Look for Plasmodium parasites.
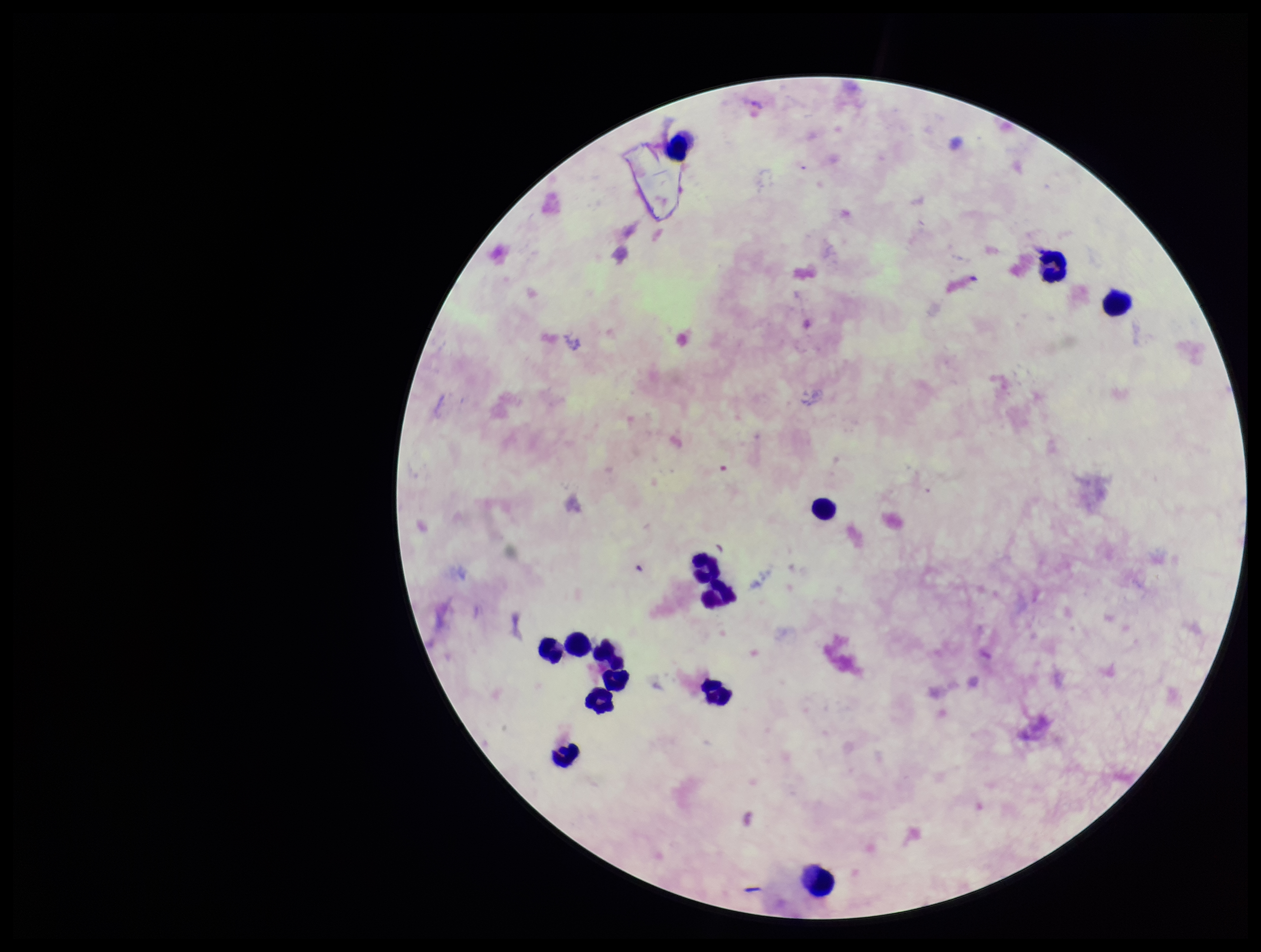

None detected.

Summary:
  - Field of view: one from this slide
  - Parasite count: 0
  - Species reported for this patient: Plasmodium vivax
  - Image size: 1261×952 pixels
  - Stain: Giemsa
  - Patient malaria status: positive
  - Leukocyte count: 14
  - Preparation: thick
  - Capture: smartphone photograph through the microscope eyepiece